State the blood parasite species.
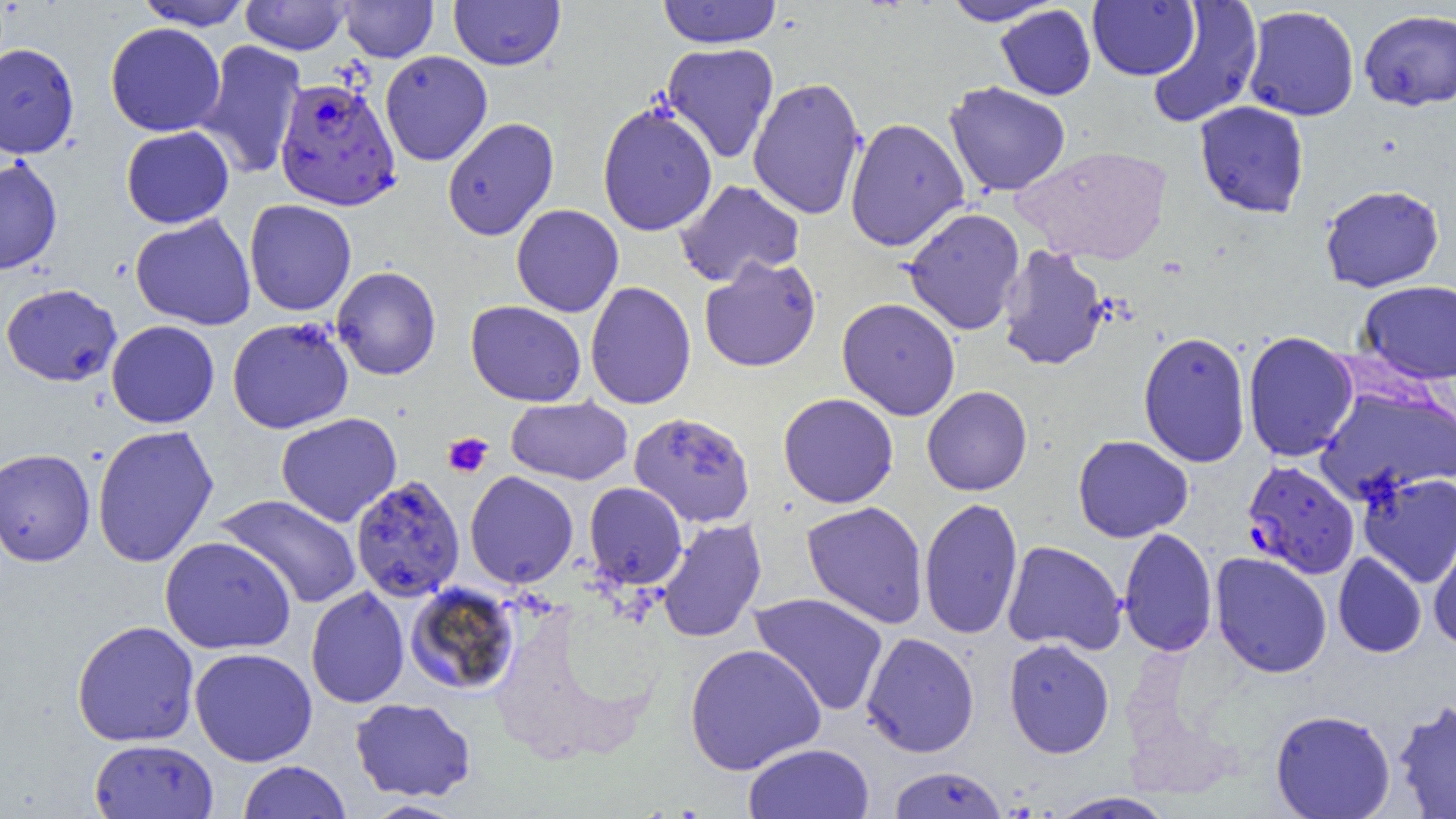
Plasmodium falciparum.

modality = light microscopy
field of view = single
uninfected red blood cell locations = approximate bounding boxes as named x1/y1/x2/y2 corners in pixels: (x1=135, y1=0, x2=253, y2=31), (x1=240, y1=0, x2=351, y2=55), (x1=657, y1=0, x2=782, y2=49), (x1=942, y1=0, x2=1060, y2=26), (x1=339, y1=1, x2=438, y2=62), (x1=449, y1=1, x2=565, y2=70), (x1=1087, y1=1, x2=1199, y2=81), (x1=1146, y1=1, x2=1263, y2=130), (x1=995, y1=4, x2=1096, y2=100), (x1=1242, y1=5, x2=1360, y2=121), (x1=1359, y1=9, x2=1456, y2=110), (x1=105, y1=22, x2=226, y2=137), (x1=194, y1=39, x2=307, y2=178), (x1=0, y1=42, x2=79, y2=158), (x1=661, y1=43, x2=779, y2=163), (x1=379, y1=50, x2=492, y2=166), (x1=748, y1=77, x2=867, y2=220), (x1=944, y1=81, x2=1071, y2=197), (x1=1194, y1=101, x2=1309, y2=218), (x1=597, y1=103, x2=718, y2=236), (x1=442, y1=117, x2=559, y2=242), (x1=844, y1=117, x2=969, y2=252), (x1=121, y1=126, x2=234, y2=228), (x1=1013, y1=145, x2=1172, y2=265), (x1=0, y1=156, x2=62, y2=275), (x1=674, y1=179, x2=805, y2=287), (x1=1320, y1=184, x2=1445, y2=293), (x1=244, y1=198, x2=357, y2=315), (x1=511, y1=204, x2=624, y2=317), (x1=903, y1=207, x2=1025, y2=336), (x1=130, y1=213, x2=256, y2=330), (x1=998, y1=244, x2=1110, y2=371), (x1=699, y1=255, x2=822, y2=372), (x1=331, y1=266, x2=441, y2=380), (x1=1357, y1=280, x2=1456, y2=385), (x1=585, y1=281, x2=696, y2=410), (x1=1, y1=283, x2=122, y2=386), (x1=837, y1=297, x2=961, y2=421), (x1=466, y1=300, x2=586, y2=406), (x1=227, y1=317, x2=354, y2=434), (x1=106, y1=320, x2=220, y2=428), (x1=1138, y1=330, x2=1251, y2=468), (x1=1242, y1=331, x2=1358, y2=462), (x1=1315, y1=384, x2=1455, y2=505), (x1=922, y1=385, x2=1032, y2=496), (x1=778, y1=392, x2=899, y2=508), (x1=791, y1=394, x2=904, y2=628), (x1=505, y1=396, x2=632, y2=485), (x1=629, y1=411, x2=755, y2=527), (x1=276, y1=412, x2=402, y2=527), (x1=92, y1=424, x2=218, y2=567), (x1=1072, y1=435, x2=1194, y2=542), (x1=0, y1=448, x2=95, y2=566), (x1=464, y1=471, x2=578, y2=588), (x1=1357, y1=472, x2=1456, y2=588), (x1=350, y1=476, x2=465, y2=602), (x1=584, y1=482, x2=687, y2=589), (x1=216, y1=494, x2=361, y2=609), (x1=919, y1=496, x2=1023, y2=640), (x1=802, y1=501, x2=928, y2=628), (x1=657, y1=518, x2=767, y2=643), (x1=1118, y1=527, x2=1218, y2=657), (x1=1428, y1=528, x2=1456, y2=650), (x1=159, y1=536, x2=296, y2=655), (x1=1002, y1=540, x2=1126, y2=655), (x1=1210, y1=552, x2=1332, y2=678), (x1=1333, y1=552, x2=1427, y2=657), (x1=404, y1=582, x2=521, y2=695), (x1=306, y1=586, x2=410, y2=708), (x1=749, y1=592, x2=889, y2=716), (x1=72, y1=620, x2=199, y2=746), (x1=861, y1=631, x2=979, y2=758), (x1=1003, y1=638, x2=1115, y2=758), (x1=684, y1=643, x2=826, y2=775), (x1=189, y1=647, x2=318, y2=766), (x1=350, y1=697, x2=476, y2=802), (x1=1393, y1=699, x2=1456, y2=818), (x1=1270, y1=709, x2=1396, y2=819), (x1=89, y1=738, x2=219, y2=818), (x1=743, y1=743, x2=874, y2=818), (x1=238, y1=760, x2=351, y2=818), (x1=887, y1=766, x2=1007, y2=818), (x1=1046, y1=791, x2=1178, y2=818), (x1=360, y1=800, x2=469, y2=818)
image size = 1456×819 pixels
preparation = thin blood film
platelet locations = approximate bounding boxes as named x1/y1/x2/y2 corners in pixels: (x1=443, y1=432, x2=493, y2=477)
magnification = 1000x
Plasmodium falciparum-infected red blood cell locations = approximate bounding boxes as named x1/y1/x2/y2 corners in pixels: (x1=274, y1=77, x2=401, y2=211), (x1=1242, y1=460, x2=1360, y2=579)